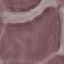
Summary:
  - Result: negative for malaria parasites
  - Capture: smartphone through the microscope eyepiece
  - Image type: automatically extracted cell patch, resized to 64 × 64 pixels
  - Stain: Giemsa
  - Preparation: thin blood smear